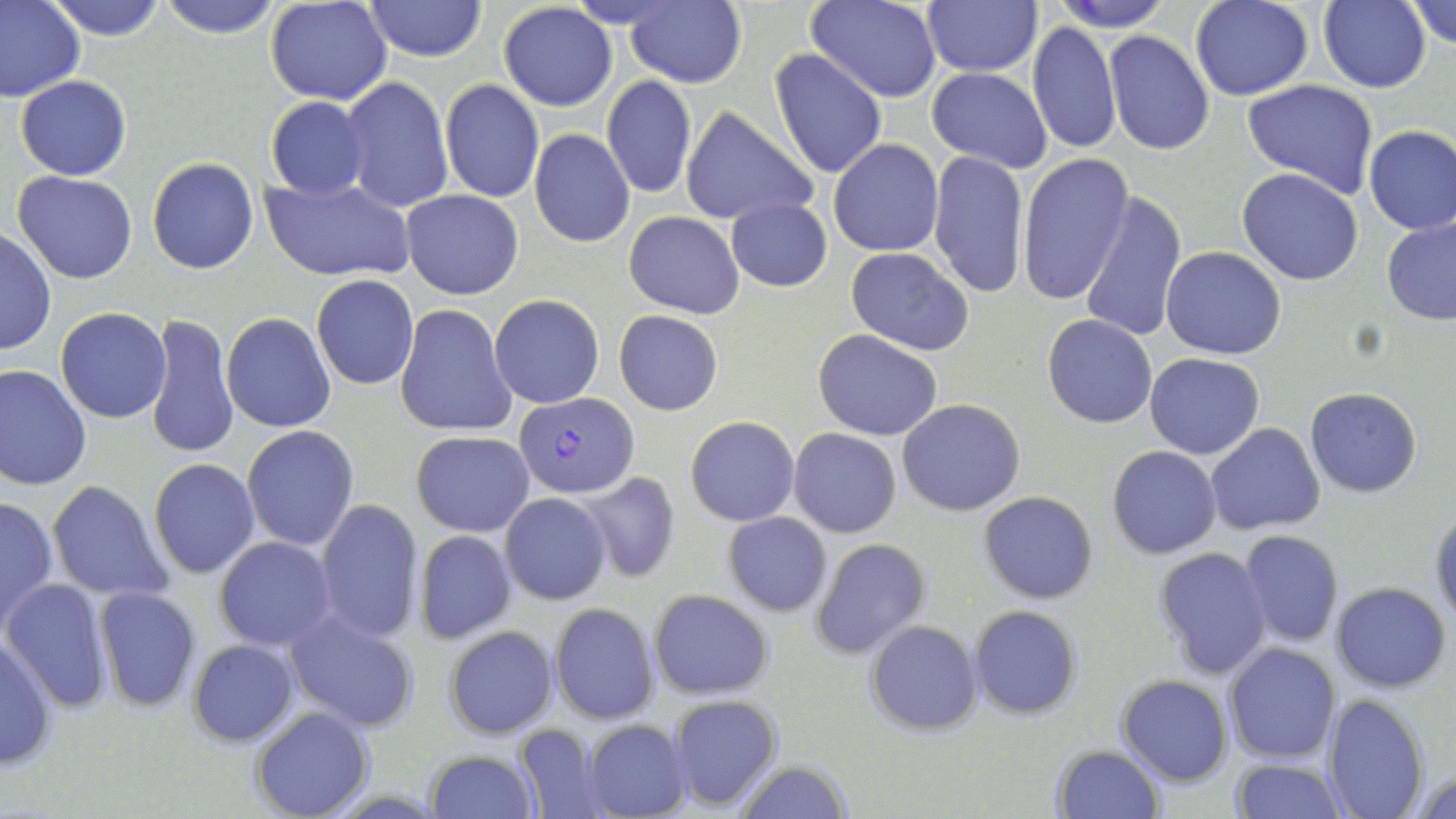

Approximate bounding boxes as (x1,y1)-(x2,y2) corner pairs in pixels. Uninfected red blood cell locations: (45,0)-(170,40), (157,0)-(282,38), (266,0)-(392,105), (624,0)-(746,87), (806,0)-(942,104), (921,0)-(1042,76), (1047,0)-(1176,32), (1189,0)-(1312,101), (1318,0)-(1431,92), (1405,0)-(1456,48), (0,1)-(85,102), (366,1)-(487,63), (497,2)-(617,112), (1028,21)-(1121,156), (1104,32)-(1214,155), (770,49)-(888,180), (927,66)-(1052,174), (16,76)-(131,180), (339,76)-(453,215), (601,76)-(698,199), (439,79)-(544,203), (1243,79)-(1379,199), (265,97)-(370,200), (680,106)-(818,228), (1363,125)-(1456,234), (529,129)-(635,248), (829,139)-(943,256), (928,150)-(1028,298), (1017,151)-(1133,304), (147,157)-(260,274), (1238,168)-(1363,285), (12,171)-(138,284), (262,175)-(414,282), (402,190)-(524,299), (1079,191)-(1186,342), (726,197)-(833,293), (625,211)-(744,317), (1381,218)-(1456,325), (0,229)-(55,357), (1161,246)-(1285,360), (845,247)-(974,355), (311,274)-(419,389), (489,294)-(605,408), (394,304)-(517,438), (56,308)-(171,423), (614,310)-(722,415), (145,311)-(240,459), (222,312)-(335,432), (1043,315)-(1157,428), (814,330)-(943,441), (1145,353)-(1265,458), (0,363)-(92,490), (1304,388)-(1422,498), (898,398)-(1024,516), (686,416)-(799,526), (1207,423)-(1325,534), (242,424)-(358,550), (789,428)-(901,538), (411,430)-(533,536), (148,442)-(356,565), (1107,446)-(1221,559), (148,458)-(260,578), (574,472)-(681,583), (48,480)-(174,602), (501,492)-(611,605), (979,492)-(1099,605), (1,496)-(59,632), (315,498)-(425,643), (1429,505)-(1455,627), (723,511)-(831,616), (414,529)-(517,644), (1237,530)-(1344,648), (214,536)-(338,650), (810,538)-(931,659), (1153,548)-(1272,679), (2,578)-(115,711), (1332,581)-(1451,692), (93,585)-(202,711), (649,589)-(773,700), (548,603)-(661,725), (969,605)-(1081,717), (283,606)-(420,732), (865,620)-(981,736), (444,626)-(560,738), (0,634)-(58,774), (188,639)-(300,746), (1225,643)-(1342,765), (1117,673)-(1233,786), (1322,693)-(1429,819), (667,694)-(783,811), (251,706)-(375,819), (583,719)-(692,819), (514,724)-(611,819), (1050,745)-(1163,819), (424,749)-(539,818), (1231,759)-(1345,818), (730,760)-(853,818), (1412,763)-(1456,819). Plasmodium falciparum-infected red blood cell locations: (514,392)-(639,497). Slide-level diagnosis: Plasmodium falciparum. One field of a larger specimen. May-Grünwald-Giemsa-stained preparation. 1000x magnification. Thin blood film. Image is 1456×819 pixels. Optical microscopy.